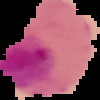

From a thin blood smear. Image is 100×100 pixels. Result: Plasmodium parasites identified. Cell region segmented out of the field of view; the surrounding area is masked to black.